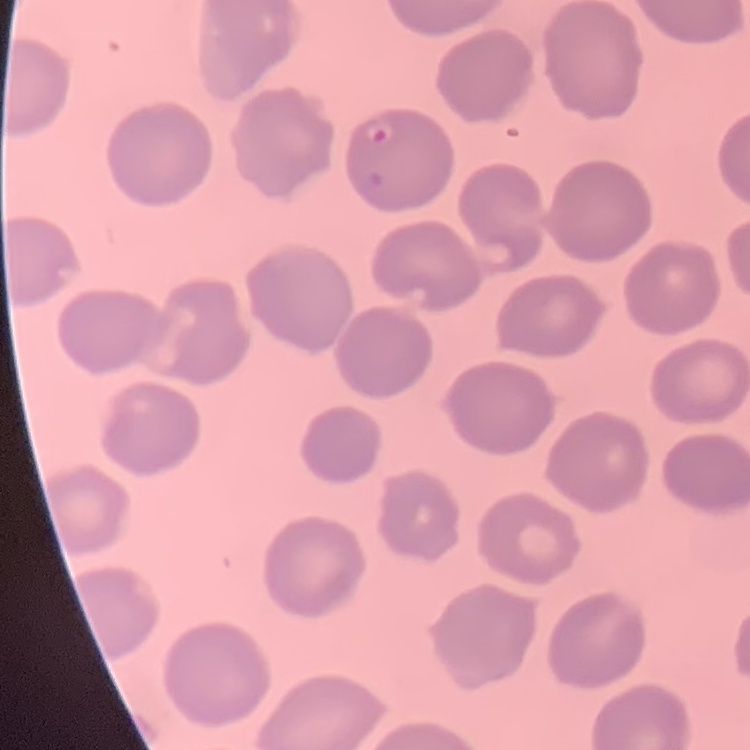
erythrocyte morphology = no rouleaux formation
preparation = thin blood film
stain = Field's or Giemsa
image type = one tile cut from a larger photomicrograph